Name the blood parasite species.
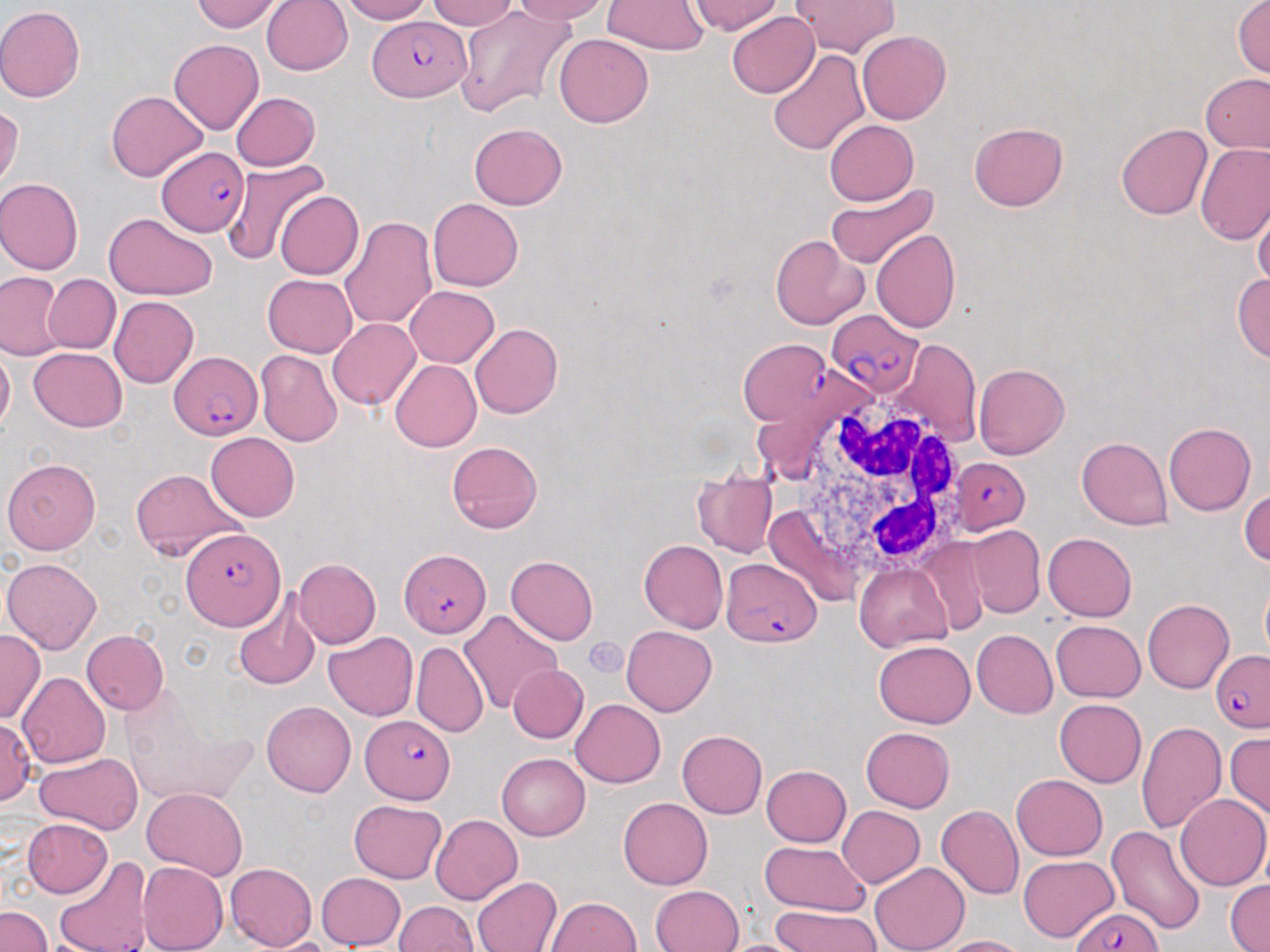

Plasmodium falciparum.

Approximate bounding boxes as [x1, y1, x2, y2] in pixels. Platelet locations: [584, 638, 627, 679]. Plasmodium falciparum-infected red blood cell locations: [372, 16, 469, 100], [157, 146, 248, 237], [826, 310, 922, 400], [739, 337, 832, 426], [170, 352, 263, 439], [951, 457, 1030, 534], [183, 529, 285, 629], [400, 549, 491, 637], [721, 558, 822, 646], [1210, 650, 1270, 732], [361, 716, 456, 802], [1074, 906, 1164, 951]. Uninfected red blood cell locations: [192, 0, 284, 33], [261, 0, 352, 75], [338, 0, 432, 23], [426, 0, 518, 30], [512, 0, 611, 23], [688, 0, 782, 35], [1232, 0, 1270, 78], [792, 1, 901, 58], [602, 2, 709, 54], [452, 4, 575, 118], [0, 5, 86, 102], [727, 12, 818, 98], [857, 30, 951, 124], [553, 34, 652, 127], [169, 39, 263, 135], [768, 49, 869, 155], [1201, 73, 1270, 154], [105, 90, 208, 182], [231, 91, 320, 170], [0, 104, 23, 191], [824, 119, 919, 206], [968, 122, 1068, 211], [470, 123, 567, 208], [1115, 123, 1213, 219], [1197, 146, 1270, 244], [222, 160, 328, 267], [0, 178, 83, 275], [826, 183, 938, 271], [276, 191, 363, 278], [427, 198, 523, 291], [1252, 202, 1270, 292], [104, 212, 218, 301], [339, 217, 437, 331], [871, 230, 960, 333], [770, 234, 869, 330], [1233, 273, 1270, 362], [1, 274, 66, 357], [44, 274, 121, 353], [262, 274, 357, 356], [405, 286, 498, 367], [109, 296, 198, 388], [327, 318, 421, 410], [470, 323, 563, 418], [890, 338, 980, 446], [0, 345, 14, 434], [28, 347, 127, 431], [255, 350, 342, 447], [389, 359, 481, 452], [974, 363, 1070, 459], [1164, 423, 1255, 516], [205, 433, 299, 522], [1077, 436, 1172, 530], [447, 440, 542, 534], [2, 459, 100, 554], [130, 467, 244, 561], [692, 473, 777, 557], [1240, 489, 1269, 568], [966, 526, 1045, 617], [1043, 532, 1137, 621], [918, 537, 994, 636], [639, 539, 728, 634], [506, 556, 598, 644], [2, 557, 102, 653], [293, 557, 381, 649], [855, 562, 952, 651], [1260, 575, 1270, 665], [232, 591, 321, 690], [1143, 599, 1233, 693], [459, 608, 562, 714], [1051, 620, 1146, 703], [622, 625, 717, 716], [0, 629, 44, 724], [81, 629, 169, 715], [972, 629, 1058, 718], [324, 632, 418, 720], [873, 640, 975, 728], [412, 642, 488, 738], [509, 664, 588, 743], [18, 672, 110, 767], [121, 695, 252, 807], [569, 698, 665, 787], [1053, 698, 1146, 788], [262, 701, 356, 797], [1, 718, 35, 806], [1136, 722, 1227, 834], [860, 727, 955, 812], [676, 730, 767, 819], [1225, 732, 1270, 822], [35, 751, 142, 833], [497, 753, 590, 841], [760, 765, 851, 847], [1011, 774, 1107, 861], [142, 786, 248, 882], [1176, 793, 1269, 891], [618, 798, 712, 890], [349, 800, 446, 883], [936, 805, 1024, 899], [837, 806, 924, 887], [431, 815, 523, 904], [22, 818, 112, 899], [1106, 826, 1206, 933], [758, 841, 871, 916], [1018, 855, 1118, 942], [53, 856, 153, 952], [138, 861, 228, 952], [869, 862, 969, 952], [225, 863, 317, 950], [315, 873, 407, 950], [471, 876, 562, 952], [1225, 881, 1269, 951], [650, 884, 744, 952], [547, 897, 641, 952], [395, 901, 480, 952], [770, 905, 881, 952], [0, 906, 51, 952], [929, 935, 1030, 952], [711, 938, 814, 952]. White blood cell locations: [784, 396, 972, 590]. Captured at 1000x magnification. May-Grünwald-Giemsa stain. Image is 1270×952 pixels. Light microscopy. Thin blood smear. Single field of view.